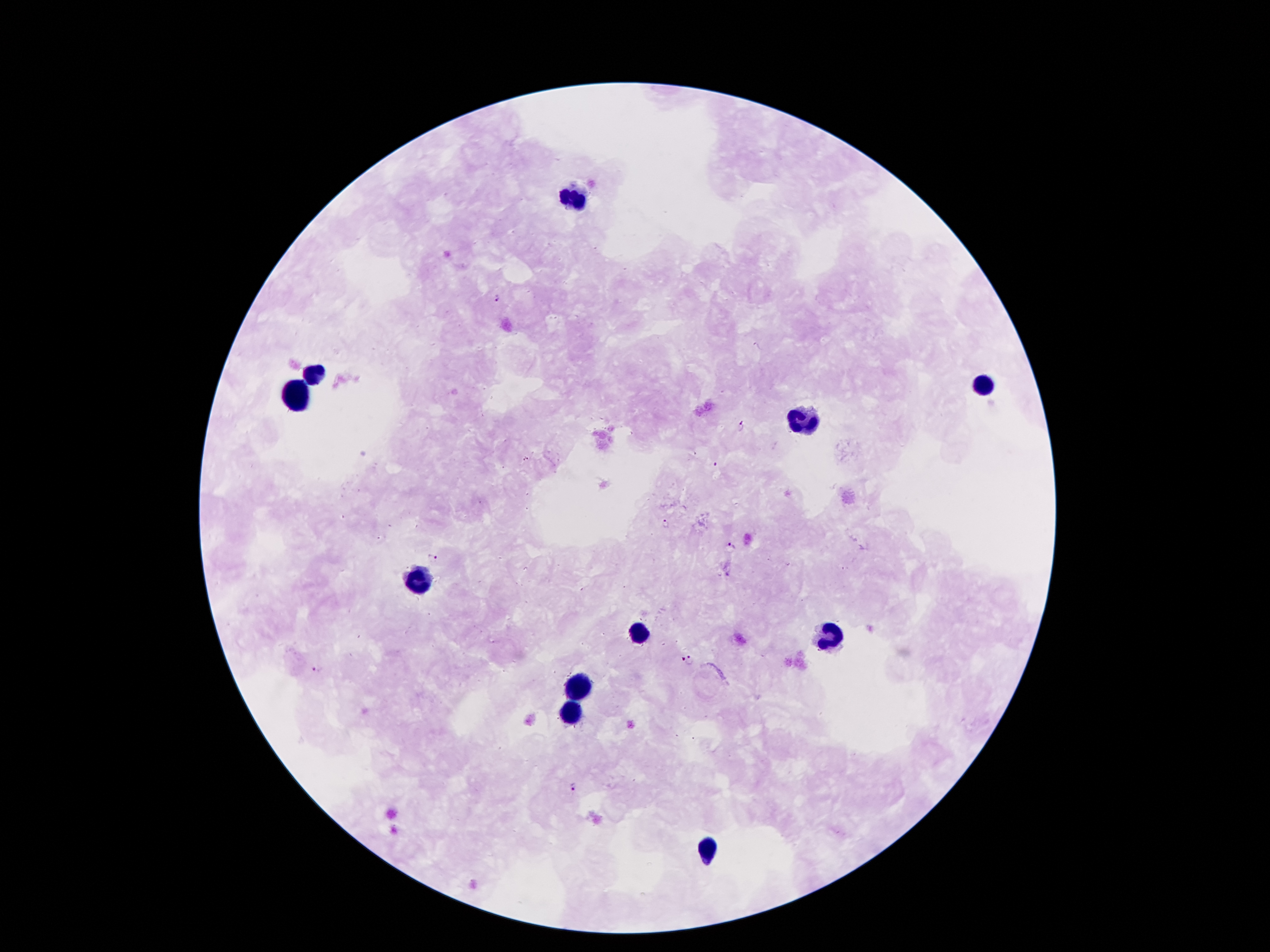

Approximate object centers, in pixels from the top-left corner. Leukocyte locations: (x=572, y=197), (x=315, y=375), (x=984, y=385), (x=298, y=395), (x=806, y=422), (x=417, y=576), (x=638, y=630), (x=831, y=633), (x=579, y=685), (x=572, y=714), (x=708, y=848). Plasmodium parasite locations: (x=498, y=295), (x=740, y=428), (x=525, y=458), (x=715, y=465), (x=665, y=524), (x=731, y=546), (x=434, y=557), (x=679, y=657), (x=689, y=660), (x=317, y=668), (x=572, y=786). Image is 1270×952 pixels. Thick blood smear. 100x magnification. Patient malaria status: positive for Plasmodium falciparum. Single field of view. Smartphone photograph taken through the microscope eyepiece. Giemsa-stained preparation.